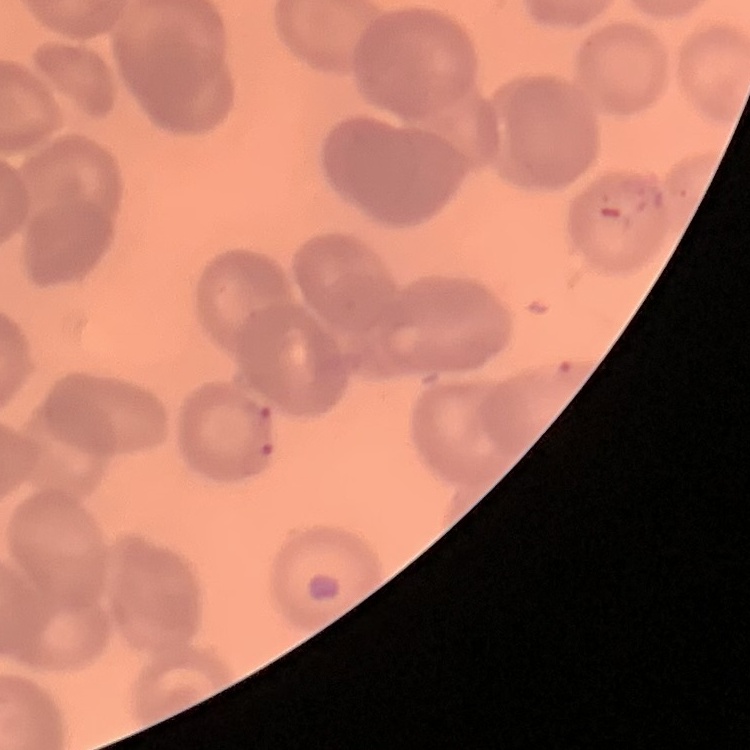
{
  "red_blood_cell_morphology": "no rouleaux formation",
  "preparation": "thin blood smear",
  "image_type": "one tile cut from a larger photomicrograph",
  "stain": "Field's or Giemsa"
}